Assess the morphology of the red blood cells.
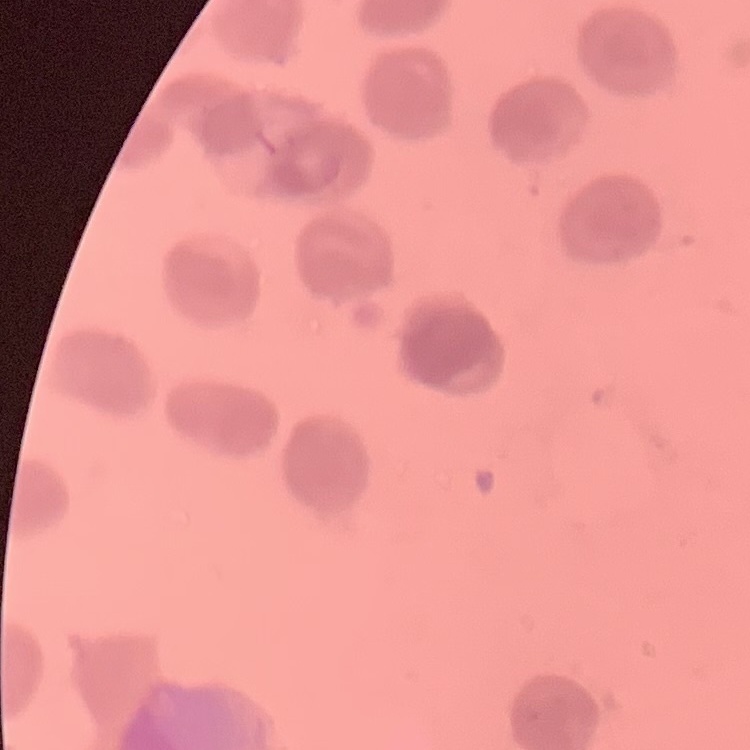
They show no rouleaux formation.

stain = Field's or Giemsa
image type = square crop of a larger photomicrograph
preparation = thin blood film